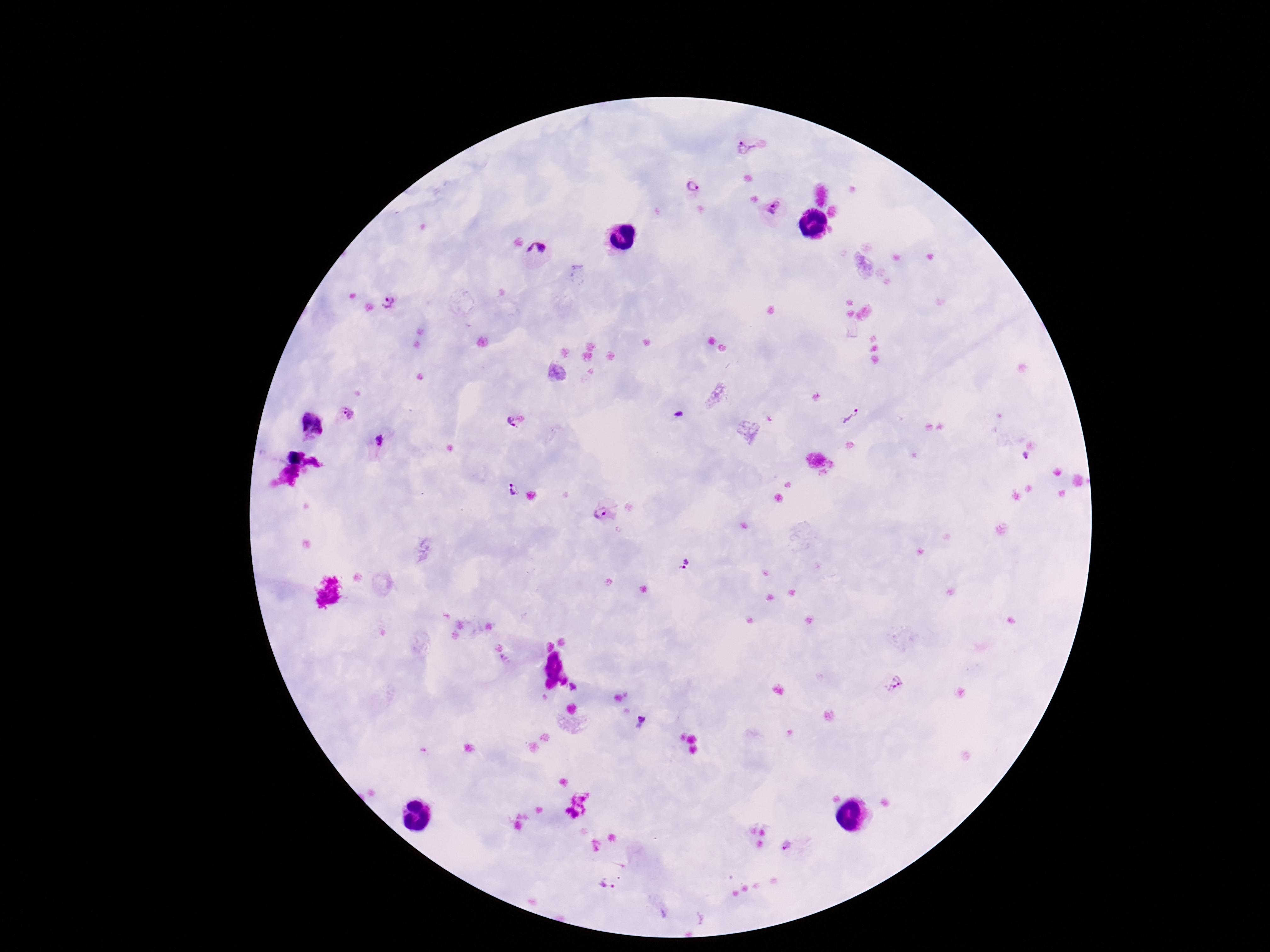

capture = smartphone camera through the microscope eyepiece
magnification = 100x
patient malaria status = infected
preparation = thick blood smear
stain = Giemsa
field of view = one from this slide
Plasmodium parasite locations = approximate centers as (x, y) in pixels: (748, 145), (690, 187), (772, 207), (537, 251), (388, 300), (679, 412), (347, 413), (850, 416), (518, 421), (313, 426), (379, 441), (1025, 456), (511, 489), (604, 512), (684, 565), (892, 684), (641, 720), (785, 845), (607, 885)
image size = 1270×952 pixels